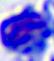 Photomicrograph. A leukocyte is seen. 400x magnification.